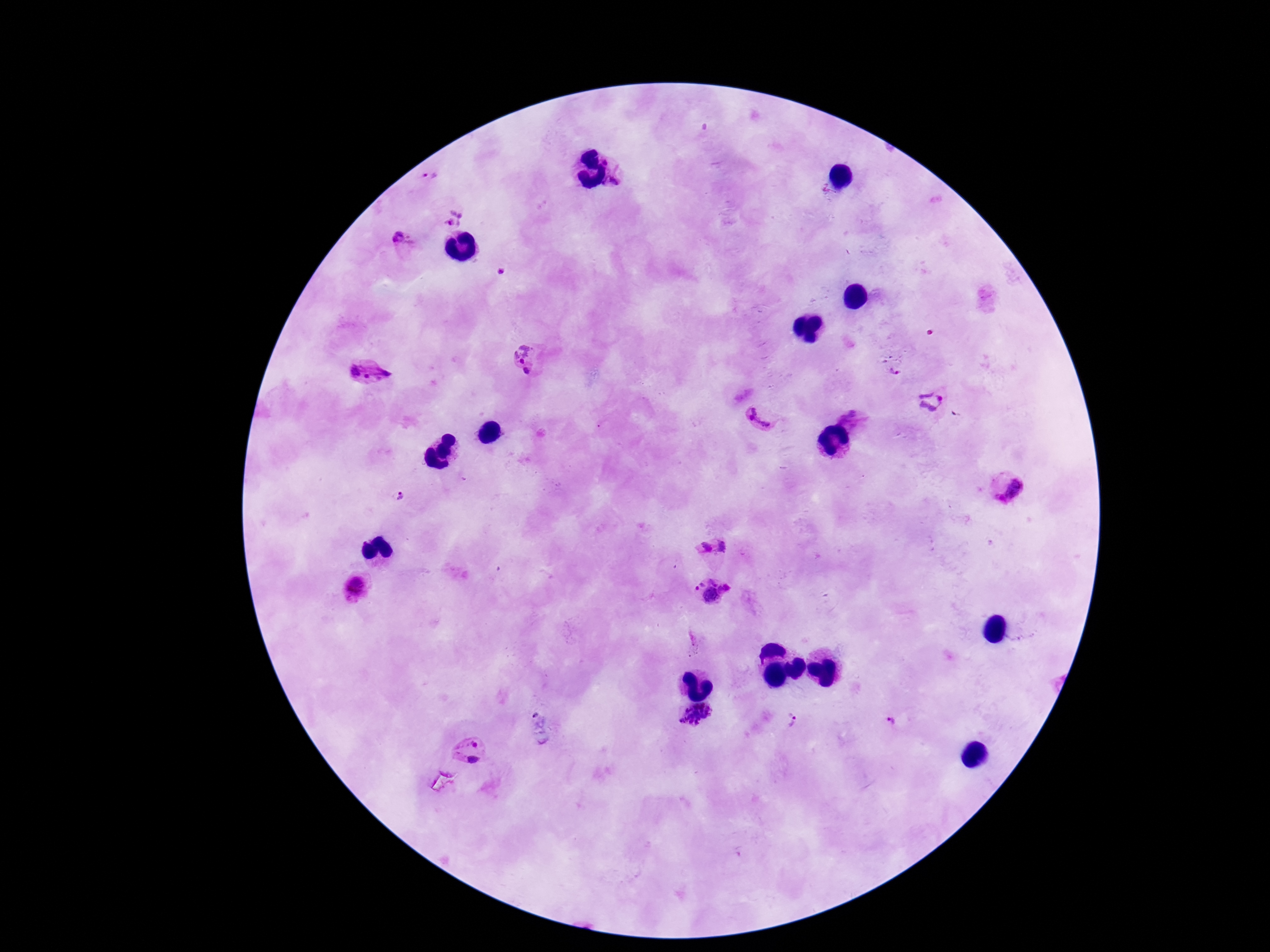
preparation = thick blood film
Plasmodium parasite locations = approximate centers as {x, y} in pixels: {609, 157}, {429, 176}, {611, 184}, {454, 216}, {404, 244}, {500, 271}, {527, 361}, {894, 369}, {367, 373}, {933, 401}, {762, 416}, {853, 419}, {1004, 484}, {399, 496}, {723, 546}, {702, 548}, {358, 586}, {709, 590}, {696, 717}, {793, 721}, {893, 722}, {467, 752}
image size = 1270×952 pixels
capture = smartphone camera through the microscope eyepiece
stain = Giemsa
field of view = one from this slide
magnification = 100x
patient malaria status = infected